Classify this cell by malaria status.
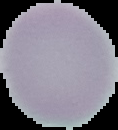

It is uninfected.

Summary:
  - Image size: 118×130 pixels
  - Image type: segmented cell region on a black background
  - Preparation: thin blood smear